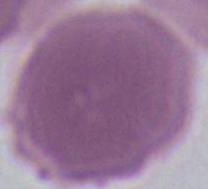

Summary:
  - Identification: erythrocyte
  - Modality: micrograph
  - Magnification: 1000x